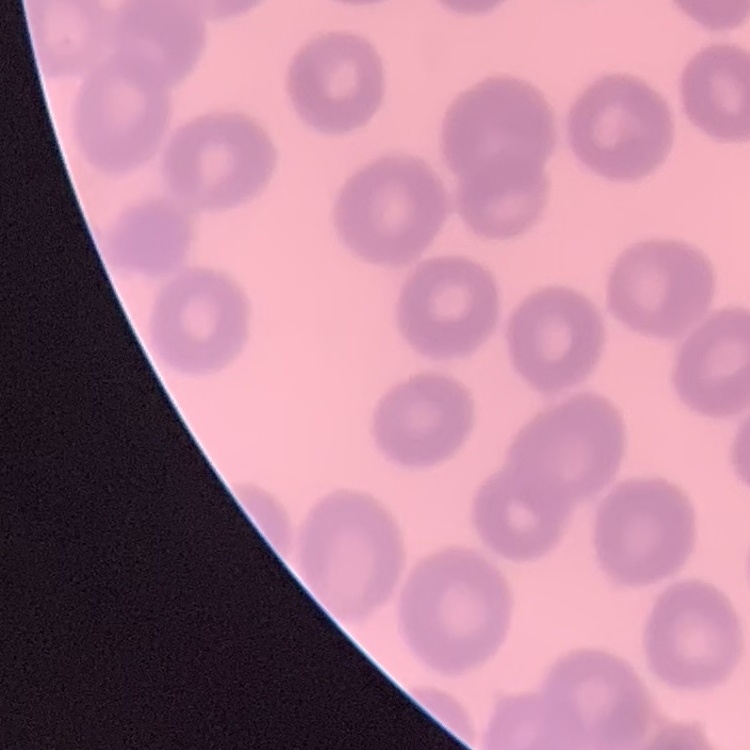

red blood cell morphology = no rouleaux formation
image type = square crop of a larger photomicrograph
preparation = thin peripheral smear
stain = Field's or Giemsa